Report the malaria status of this cell.
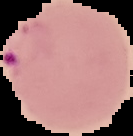

It is parasitized.

Image is 133×136 pixels. Cell region segmented out of the field of view; the surrounding area is masked to black. From a thin blood film.